Classify this cell by malaria status.
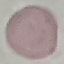

It is uninfected.

{
  "image_type": "cell patch, automatically extracted from a larger field of view and resized to 64 × 64 pixels",
  "stain": "Giemsa",
  "preparation": "thin blood film",
  "capture": "smartphone camera at the microscope eyepiece"
}